Locate every Plasmodium falciparum-infected red blood cell.
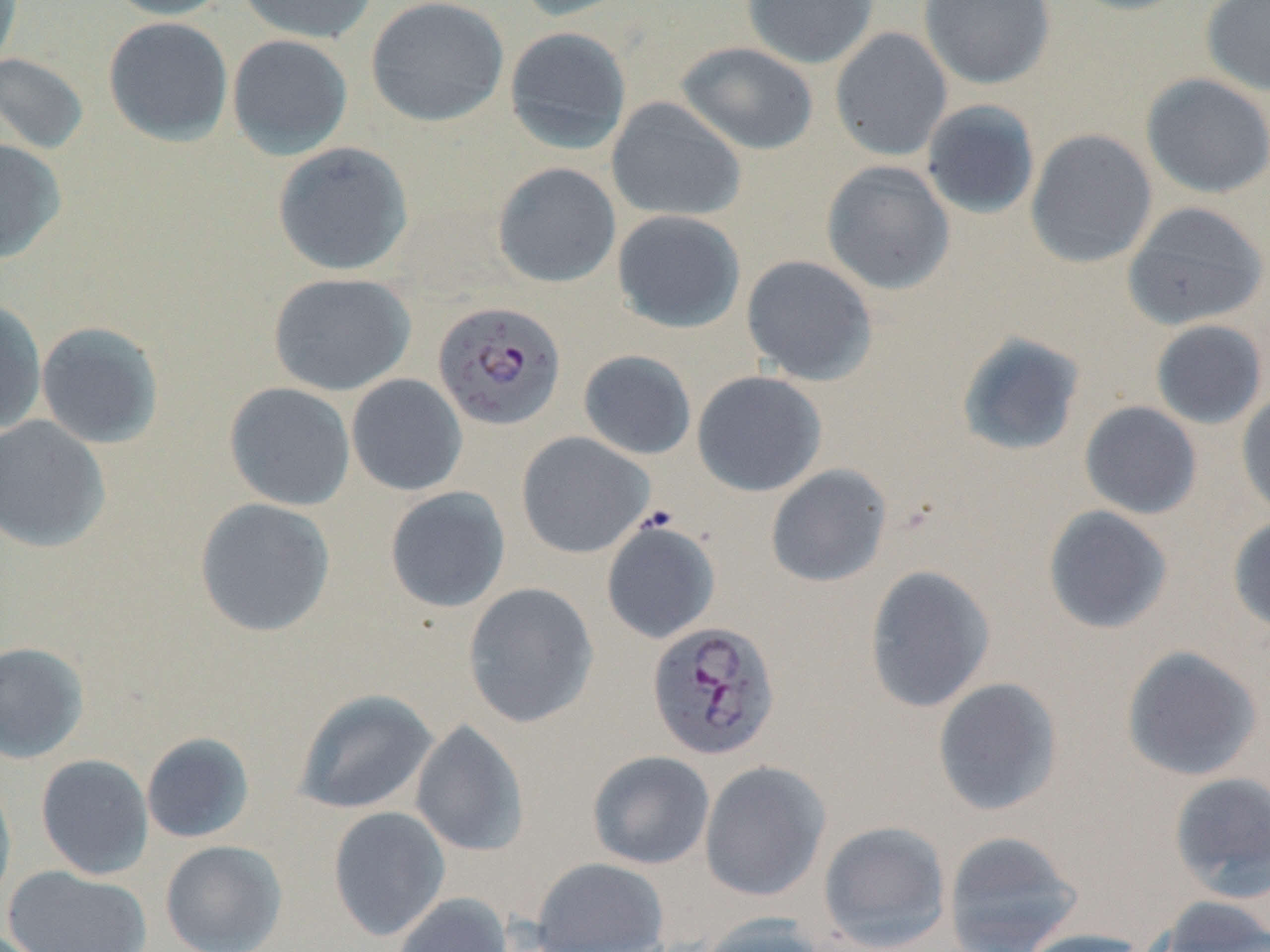
Approximate bounding boxes as (x1,y1)-(x2,y2) corner pairs in pixels.
Plasmodium falciparum-infected red blood cells: (433,300)-(566,430), (646,621)-(781,760).

Summary:
  - Uninfected red blood cell locations: (0,0)-(23,70), (101,0)-(233,20), (236,0)-(376,44), (365,0)-(510,127), (511,0)-(642,22), (741,0)-(880,69), (918,0)-(1056,89), (1064,0)-(1196,16), (1200,0)-(1270,97), (103,16)-(233,147), (504,26)-(633,154), (829,27)-(953,161), (227,34)-(353,160), (676,41)-(819,155), (0,52)-(90,155), (1140,73)-(1270,199), (606,97)-(747,222), (921,100)-(1041,220), (1025,129)-(1157,268), (0,138)-(67,265), (272,141)-(414,276), (821,160)-(956,295), (491,161)-(622,288), (1121,200)-(1270,331), (611,209)-(746,334), (741,255)-(878,386), (267,272)-(416,396), (0,298)-(47,435), (1150,319)-(1268,430), (36,320)-(165,449), (956,331)-(1086,457), (578,349)-(697,460), (692,371)-(827,496), (346,374)-(468,496), (224,382)-(356,511), (1236,390)-(1270,520), (1079,401)-(1203,520), (0,415)-(111,553), (516,432)-(654,559), (765,464)-(892,587), (384,486)-(511,613), (194,497)-(336,637), (1042,505)-(1174,635), (1227,514)-(1270,635), (600,518)-(721,644), (864,565)-(995,713), (463,582)-(599,728), (0,641)-(89,764), (1120,645)-(1264,781), (932,677)-(1064,817), (293,688)-(438,815), (410,720)-(529,857), (141,732)-(255,843), (587,750)-(715,870), (35,753)-(154,880), (699,760)-(831,901), (0,771)-(17,911), (1168,772)-(1270,901), (327,806)-(450,941), (818,820)-(951,951), (942,830)-(1083,952), (160,840)-(288,952), (531,856)-(670,951), (4,866)-(152,952), (392,892)-(513,952), (1151,896)-(1270,952), (695,913)-(828,952), (1015,928)-(1154,952)
  - Slide-level diagnosis: Plasmodium falciparum
  - Image size: 1270×952 pixels
  - Stain: May-Grünwald-Giemsa
  - Field of view: one of a larger specimen
  - Modality: light microscopy
  - Preparation: thin blood smear
  - Magnification: 1000x